Outline each blood parasite and name the species.
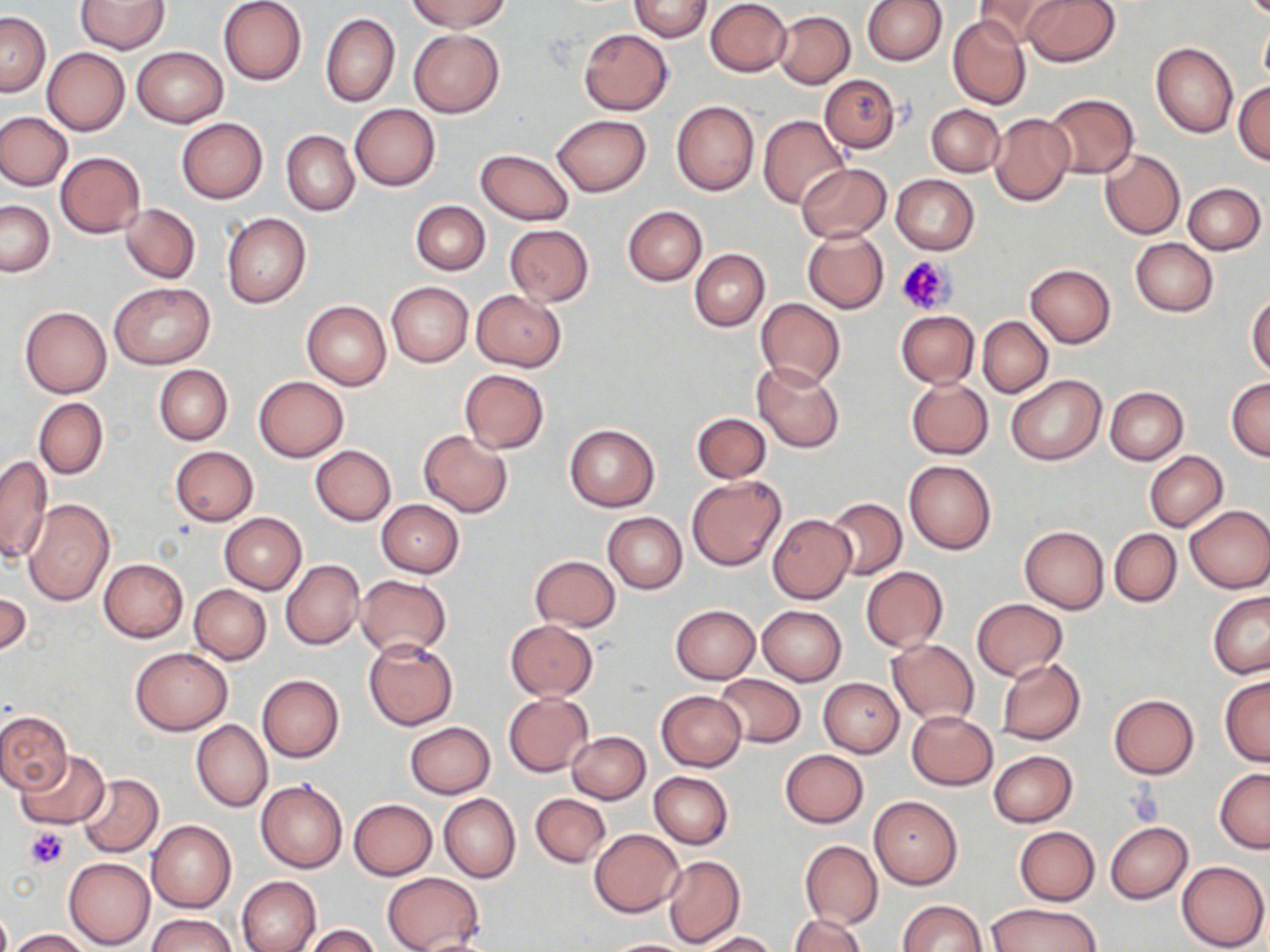

No blood parasites observed.

Approximate bounding boxes as named x1/y1/x2/y2 corners in pixels. Uninfected red blood cell locations: (x1=218, y1=0, x2=307, y2=85), (x1=409, y1=0, x2=511, y2=33), (x1=705, y1=0, x2=791, y2=76), (x1=863, y1=0, x2=947, y2=65), (x1=973, y1=0, x2=1064, y2=47), (x1=1021, y1=0, x2=1121, y2=67), (x1=76, y1=1, x2=169, y2=54), (x1=627, y1=1, x2=713, y2=41), (x1=773, y1=10, x2=854, y2=89), (x1=0, y1=12, x2=50, y2=96), (x1=320, y1=12, x2=399, y2=107), (x1=948, y1=15, x2=1031, y2=111), (x1=1259, y1=20, x2=1270, y2=88), (x1=578, y1=28, x2=674, y2=114), (x1=410, y1=29, x2=504, y2=118), (x1=1151, y1=43, x2=1238, y2=138), (x1=131, y1=46, x2=228, y2=127), (x1=42, y1=48, x2=129, y2=135), (x1=820, y1=75, x2=901, y2=153), (x1=1232, y1=82, x2=1270, y2=164), (x1=1042, y1=92, x2=1139, y2=179), (x1=672, y1=101, x2=759, y2=196), (x1=926, y1=103, x2=1004, y2=176), (x1=350, y1=104, x2=440, y2=191), (x1=0, y1=112, x2=73, y2=190), (x1=989, y1=112, x2=1074, y2=205), (x1=551, y1=114, x2=650, y2=197), (x1=758, y1=115, x2=850, y2=210), (x1=177, y1=118, x2=268, y2=204), (x1=282, y1=130, x2=359, y2=216), (x1=475, y1=148, x2=575, y2=225), (x1=1100, y1=150, x2=1184, y2=240), (x1=55, y1=151, x2=145, y2=238), (x1=797, y1=163, x2=891, y2=242), (x1=891, y1=174, x2=979, y2=254), (x1=1184, y1=182, x2=1266, y2=255), (x1=0, y1=200, x2=54, y2=276), (x1=411, y1=200, x2=490, y2=276), (x1=121, y1=204, x2=200, y2=283), (x1=623, y1=206, x2=707, y2=286), (x1=221, y1=212, x2=312, y2=308), (x1=504, y1=224, x2=593, y2=305), (x1=802, y1=228, x2=889, y2=313), (x1=1130, y1=238, x2=1218, y2=316), (x1=689, y1=249, x2=769, y2=331), (x1=1025, y1=263, x2=1116, y2=348), (x1=108, y1=280, x2=215, y2=370), (x1=386, y1=281, x2=473, y2=367), (x1=472, y1=290, x2=566, y2=371), (x1=1247, y1=293, x2=1270, y2=377), (x1=755, y1=298, x2=845, y2=389), (x1=301, y1=300, x2=391, y2=390), (x1=20, y1=306, x2=111, y2=399), (x1=896, y1=310, x2=979, y2=388), (x1=978, y1=317, x2=1053, y2=397), (x1=752, y1=362, x2=844, y2=453), (x1=153, y1=364, x2=233, y2=445), (x1=459, y1=369, x2=549, y2=453), (x1=1005, y1=373, x2=1105, y2=466), (x1=253, y1=375, x2=348, y2=461), (x1=1226, y1=376, x2=1270, y2=461), (x1=907, y1=378, x2=993, y2=459), (x1=1105, y1=386, x2=1188, y2=464), (x1=34, y1=398, x2=108, y2=480), (x1=692, y1=412, x2=770, y2=482), (x1=563, y1=424, x2=660, y2=511), (x1=419, y1=430, x2=513, y2=517), (x1=310, y1=445, x2=396, y2=525), (x1=170, y1=446, x2=258, y2=525), (x1=1145, y1=451, x2=1228, y2=532), (x1=0, y1=455, x2=52, y2=566), (x1=903, y1=460, x2=996, y2=554), (x1=686, y1=476, x2=786, y2=571), (x1=23, y1=498, x2=115, y2=605), (x1=825, y1=498, x2=906, y2=579), (x1=375, y1=500, x2=464, y2=577), (x1=1184, y1=504, x2=1270, y2=593), (x1=219, y1=512, x2=306, y2=594), (x1=602, y1=512, x2=687, y2=593), (x1=767, y1=514, x2=855, y2=603), (x1=1020, y1=526, x2=1109, y2=614), (x1=1109, y1=528, x2=1181, y2=607), (x1=530, y1=556, x2=620, y2=631), (x1=99, y1=558, x2=188, y2=642), (x1=281, y1=559, x2=364, y2=650), (x1=516, y1=560, x2=612, y2=699), (x1=860, y1=566, x2=948, y2=652), (x1=355, y1=575, x2=452, y2=657), (x1=188, y1=584, x2=271, y2=664), (x1=0, y1=587, x2=31, y2=658), (x1=1207, y1=592, x2=1269, y2=676), (x1=972, y1=598, x2=1066, y2=681), (x1=671, y1=605, x2=761, y2=684), (x1=757, y1=605, x2=847, y2=685), (x1=504, y1=619, x2=598, y2=701), (x1=887, y1=638, x2=979, y2=726), (x1=364, y1=639, x2=457, y2=730), (x1=129, y1=647, x2=233, y2=734), (x1=997, y1=659, x2=1086, y2=745), (x1=257, y1=674, x2=344, y2=763), (x1=715, y1=674, x2=804, y2=748), (x1=1220, y1=676, x2=1270, y2=767), (x1=819, y1=678, x2=903, y2=757), (x1=656, y1=691, x2=745, y2=772), (x1=503, y1=693, x2=592, y2=776), (x1=1108, y1=694, x2=1199, y2=778), (x1=0, y1=709, x2=73, y2=793), (x1=906, y1=711, x2=998, y2=790), (x1=191, y1=720, x2=272, y2=812), (x1=417, y1=720, x2=501, y2=870), (x1=405, y1=721, x2=495, y2=797), (x1=566, y1=731, x2=650, y2=803), (x1=780, y1=749, x2=868, y2=828), (x1=15, y1=751, x2=109, y2=831), (x1=989, y1=751, x2=1078, y2=827), (x1=1215, y1=769, x2=1270, y2=853), (x1=648, y1=771, x2=733, y2=850), (x1=77, y1=773, x2=164, y2=856), (x1=256, y1=779, x2=347, y2=872), (x1=530, y1=793, x2=609, y2=867), (x1=439, y1=794, x2=520, y2=882), (x1=869, y1=796, x2=962, y2=889), (x1=349, y1=799, x2=437, y2=880), (x1=148, y1=820, x2=236, y2=913), (x1=1104, y1=821, x2=1192, y2=903), (x1=1014, y1=826, x2=1100, y2=905), (x1=590, y1=829, x2=683, y2=916), (x1=800, y1=840, x2=883, y2=929), (x1=662, y1=855, x2=744, y2=948), (x1=63, y1=857, x2=155, y2=949), (x1=1177, y1=860, x2=1269, y2=951), (x1=381, y1=872, x2=484, y2=952), (x1=237, y1=875, x2=322, y2=952), (x1=900, y1=900, x2=987, y2=951), (x1=987, y1=902, x2=1099, y2=951), (x1=789, y1=913, x2=865, y2=951), (x1=149, y1=914, x2=235, y2=952), (x1=301, y1=925, x2=382, y2=952), (x1=7, y1=929, x2=94, y2=951), (x1=698, y1=932, x2=777, y2=952), (x1=599, y1=938, x2=697, y2=951). Platelet locations: (x1=896, y1=254, x2=955, y2=315), (x1=1129, y1=788, x2=1164, y2=826), (x1=24, y1=828, x2=69, y2=869). Slide-level diagnosis: negative for blood parasites. Thin blood smear. May-Grünwald-Giemsa stain. Light microscopy. One field of a larger specimen. Image is 1270×952 pixels. Captured at 1000x magnification.